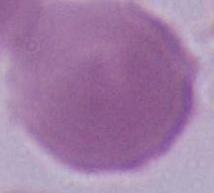

Summary:
  - Magnification: 1000x
  - Identification: red blood cell
  - Modality: photomicrograph